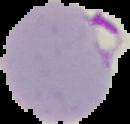
Summary:
  - Image type: segmented cell region with the area outside set to black
  - Image size: 130×124 pixels
  - Preparation: thin blood smear
  - Result: malaria parasites detected